Report the malaria status of this cell.
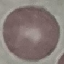

Uninfected.

Thin smear of blood. Acquired by smartphone through the microscope eyepiece. Giemsa stain. Cell patch, automatically extracted from a larger field of view and resized to 64 × 64 pixels.